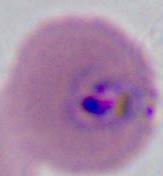

magnification = 400x or 1000x
identification = Plasmodium
modality = photomicrograph